Classify this cell by malaria status.
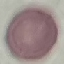
Uninfected.

Summary:
  - Image type: automatically extracted cell patch, resized to 64 × 64 pixels
  - Stain: Giemsa
  - Capture: smartphone through the microscope eyepiece
  - Preparation: thin smear